Report the malaria status of this cell.
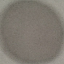
Uninfected.

Cell patch, automatically extracted from a larger field of view and resized to 64 × 64 pixels. Giemsa stain. Thin blood film. Photographed with a smartphone camera at the microscope eyepiece.